Name the parasite shown.
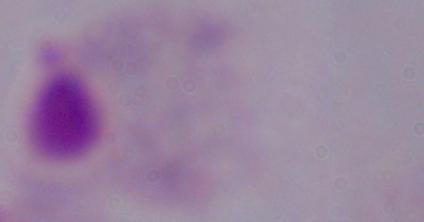

This is a trichomonad.

Summary:
  - Magnification: 1000x
  - Modality: micrograph